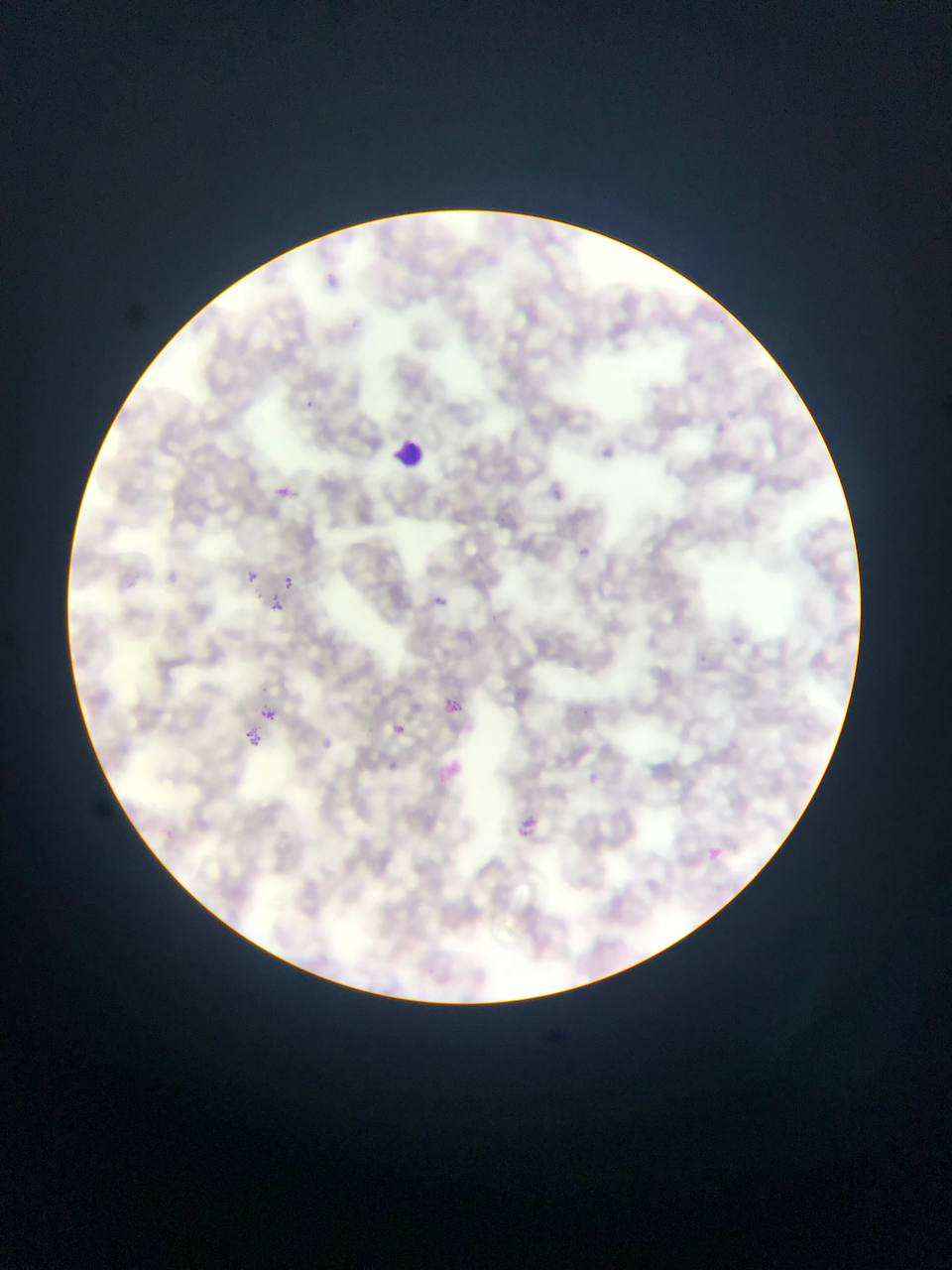
Approximate bounding boxes as [left, top, right, bottom] in pixels.
Summary:
  - Malaria parasite locations: [325, 266, 345, 296], [303, 396, 333, 419], [599, 444, 618, 469], [547, 475, 566, 505], [277, 479, 303, 507], [573, 543, 600, 563], [246, 571, 258, 582], [282, 576, 294, 588], [272, 597, 283, 611], [438, 601, 446, 615], [454, 697, 473, 721], [257, 701, 280, 720], [390, 719, 407, 743], [246, 729, 262, 745], [313, 738, 335, 749], [384, 754, 401, 771], [436, 756, 468, 783], [512, 812, 534, 841], [708, 848, 722, 860]
  - Leukocyte locations: [393, 438, 429, 470]
  - Field of view: single
  - Country: Ghana
  - Capture: mobile-phone photograph through a microscope
  - Image size: 952×1270 pixels
  - Preparation: thin blood smear